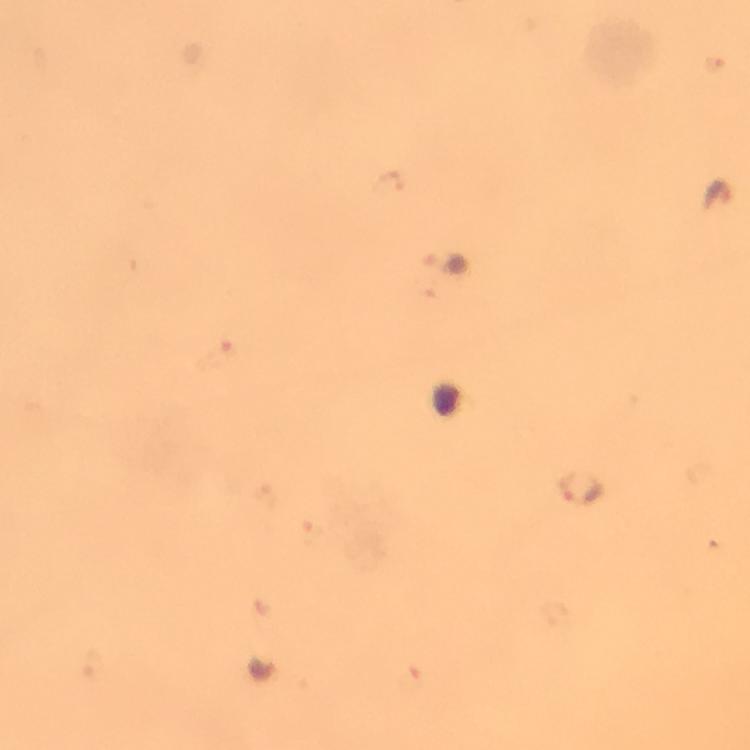
Approximate object centers, in pixels from the top-left corner.
Summary:
  - Malaria parasite locations: (x=717, y=196), (x=580, y=490), (x=264, y=668)
  - Image size: 750×750 pixels
  - Stain: Giemsa
  - Preparation: thick smear
  - Magnification: 100x
  - Capture: smartphone camera through the microscope
  - Cropped from: one field of view
  - Immersion oil: applied
  - Context: from a malaria diagnostic workup